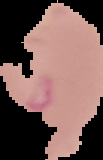

image type = segmented cell region on a black background
preparation = thin blood smear
malaria status = parasitized
image size = 103×160 pixels